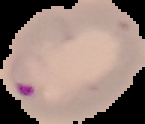
image_size: 145×124 pixels
preparation: thin blood smear
result: Plasmodium parasites identified
image_type: cell region segmented out of the field of view; surrounding area masked to black